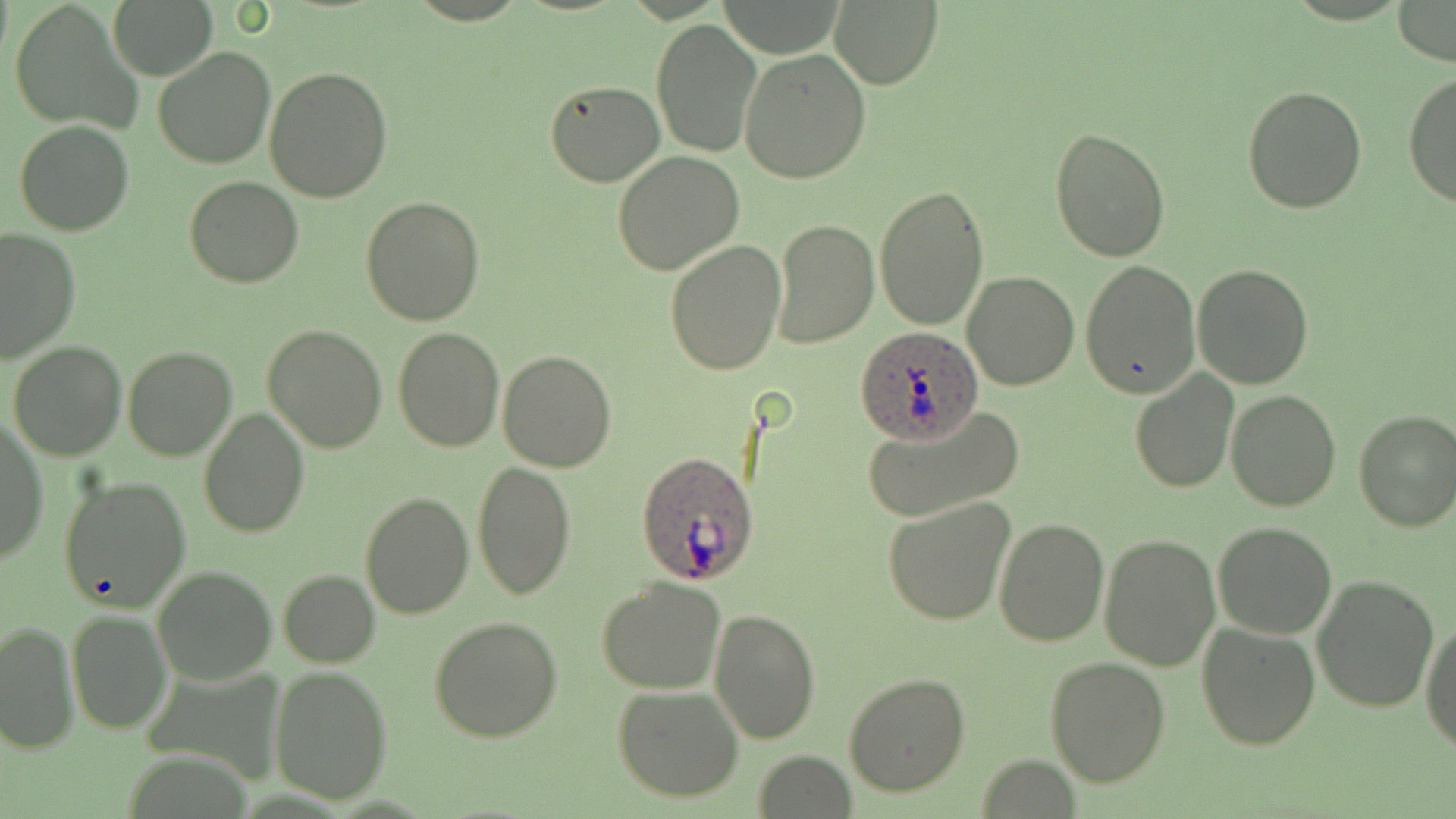 Approximate bounding boxes as named x1/y1/x2/y2 corners in pixels. Uninfected red blood cell locations: (x1=107, y1=0, x2=218, y2=81), (x1=828, y1=0, x2=943, y2=90), (x1=1391, y1=0, x2=1455, y2=66), (x1=8, y1=2, x2=142, y2=134), (x1=650, y1=17, x2=761, y2=159), (x1=738, y1=45, x2=871, y2=184), (x1=152, y1=46, x2=275, y2=169), (x1=263, y1=66, x2=394, y2=202), (x1=1404, y1=72, x2=1456, y2=210), (x1=544, y1=79, x2=667, y2=186), (x1=1242, y1=84, x2=1368, y2=214), (x1=14, y1=120, x2=134, y2=236), (x1=1049, y1=126, x2=1173, y2=263), (x1=611, y1=152, x2=745, y2=276), (x1=185, y1=177, x2=304, y2=289), (x1=875, y1=183, x2=988, y2=331), (x1=360, y1=197, x2=485, y2=325), (x1=770, y1=219, x2=878, y2=348), (x1=0, y1=228, x2=80, y2=364), (x1=664, y1=239, x2=785, y2=375), (x1=1080, y1=258, x2=1200, y2=397), (x1=1192, y1=264, x2=1313, y2=388), (x1=964, y1=270, x2=1080, y2=391), (x1=260, y1=324, x2=387, y2=452), (x1=393, y1=325, x2=503, y2=450), (x1=7, y1=340, x2=127, y2=461), (x1=123, y1=347, x2=236, y2=461), (x1=497, y1=350, x2=618, y2=471), (x1=1131, y1=370, x2=1240, y2=492), (x1=1226, y1=391, x2=1342, y2=512), (x1=860, y1=401, x2=1026, y2=524), (x1=198, y1=406, x2=309, y2=537), (x1=1352, y1=409, x2=1456, y2=531), (x1=1, y1=417, x2=48, y2=564), (x1=471, y1=459, x2=576, y2=600), (x1=59, y1=475, x2=193, y2=614), (x1=360, y1=491, x2=474, y2=619), (x1=883, y1=496, x2=1016, y2=627), (x1=992, y1=516, x2=1109, y2=647), (x1=1213, y1=522, x2=1338, y2=639), (x1=1098, y1=530, x2=1221, y2=671), (x1=151, y1=566, x2=276, y2=685), (x1=279, y1=569, x2=380, y2=667), (x1=1312, y1=573, x2=1439, y2=712), (x1=598, y1=575, x2=727, y2=694), (x1=710, y1=605, x2=820, y2=743), (x1=67, y1=611, x2=170, y2=734), (x1=429, y1=616, x2=563, y2=741), (x1=1421, y1=616, x2=1455, y2=753), (x1=1, y1=620, x2=78, y2=754), (x1=1197, y1=621, x2=1322, y2=750), (x1=1045, y1=655, x2=1171, y2=787), (x1=269, y1=666, x2=393, y2=804), (x1=842, y1=672, x2=969, y2=796), (x1=611, y1=685, x2=746, y2=802), (x1=755, y1=750, x2=856, y2=819). Plasmodium ovale-infected red blood cell locations: (x1=854, y1=327, x2=983, y2=441), (x1=636, y1=450, x2=762, y2=585). Slide-level diagnosis: Plasmodium ovale. Image is 1456×819 pixels. Thin blood film. Single field of view. Optical microscopy. May-Grünwald-Giemsa stain. 1000x magnification.